Evaluate for Plasmodium parasites.
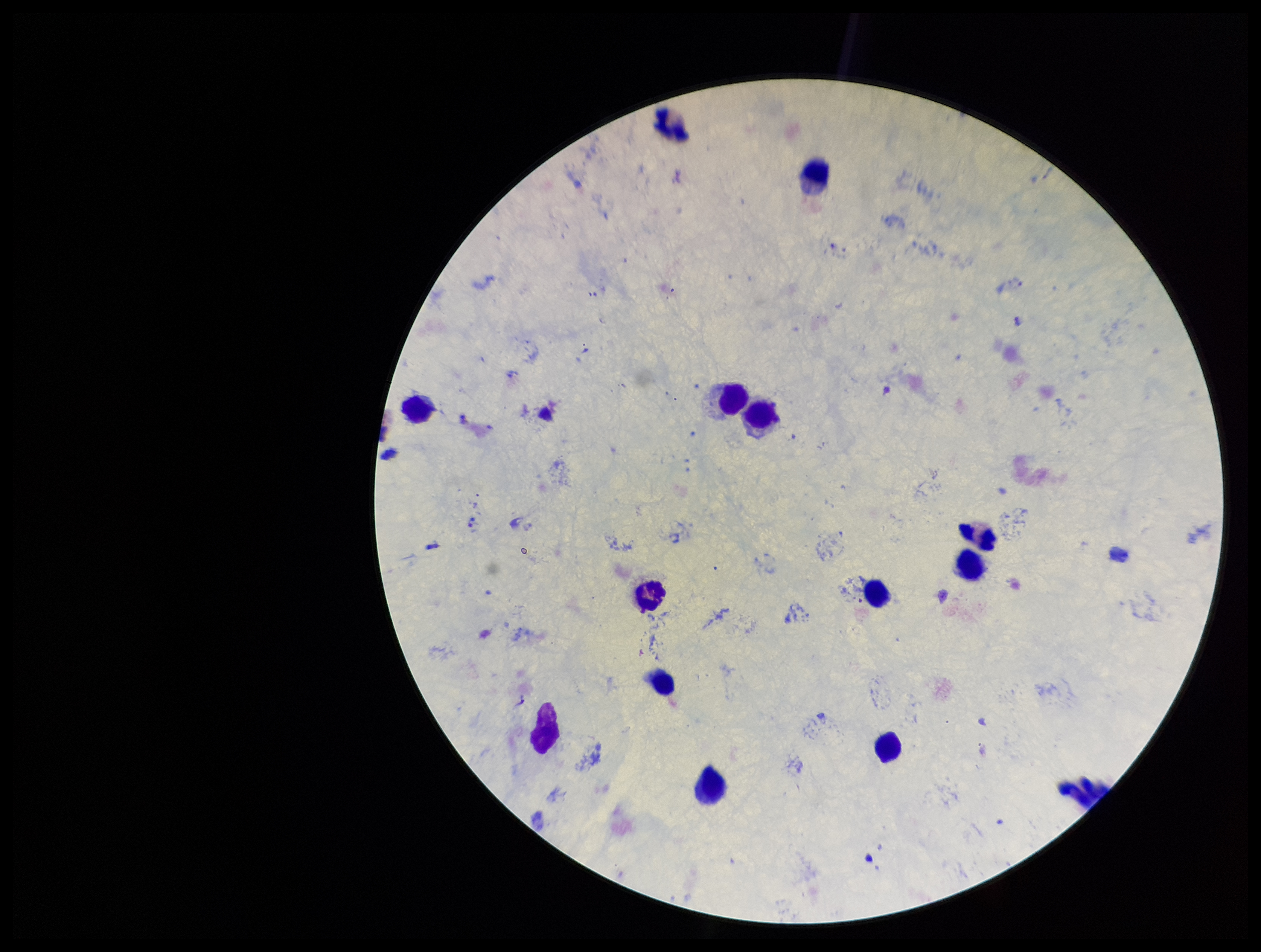

Detected.

species_reported_for_this_patient: Plasmodium vivax
image_size: 1261×952 pixels
field_of_view: single
preparation: thick blood smear
capture: smartphone photograph through the microscope eyepiece
leukocyte_count: 13
patient_malaria_status: positive
stain: Giemsa
parasite_count: 1